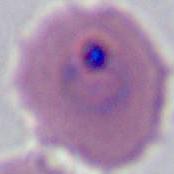
modality = photomicrograph
identification = Plasmodium
magnification = 400x or 1000x